Identify the parasite.
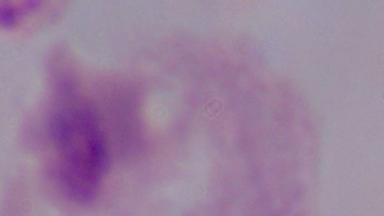

A trichomonad.

{
  "magnification": "1000x",
  "modality": "photomicrograph"
}